Assess for Plasmodium parasites.
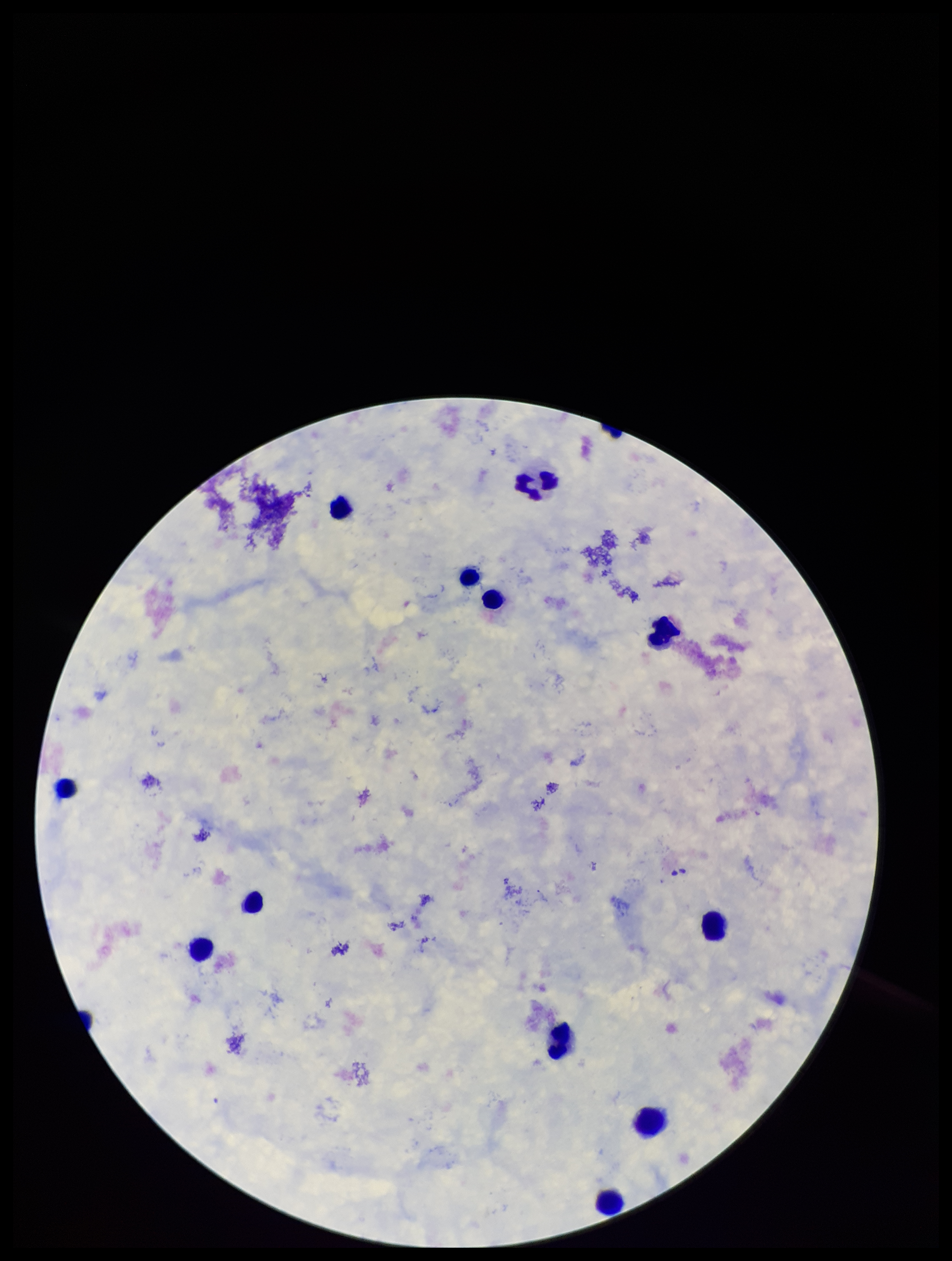
None detected.

field_of_view: one from this slide
stain: Giemsa
leukocyte_count: 10
parasite_count: 0
capture: smartphone photograph through the microscope eyepiece
preparation: thick
image_size: 952×1261 pixels
patient_malaria_status: negative